Locate and identify every blood parasite.
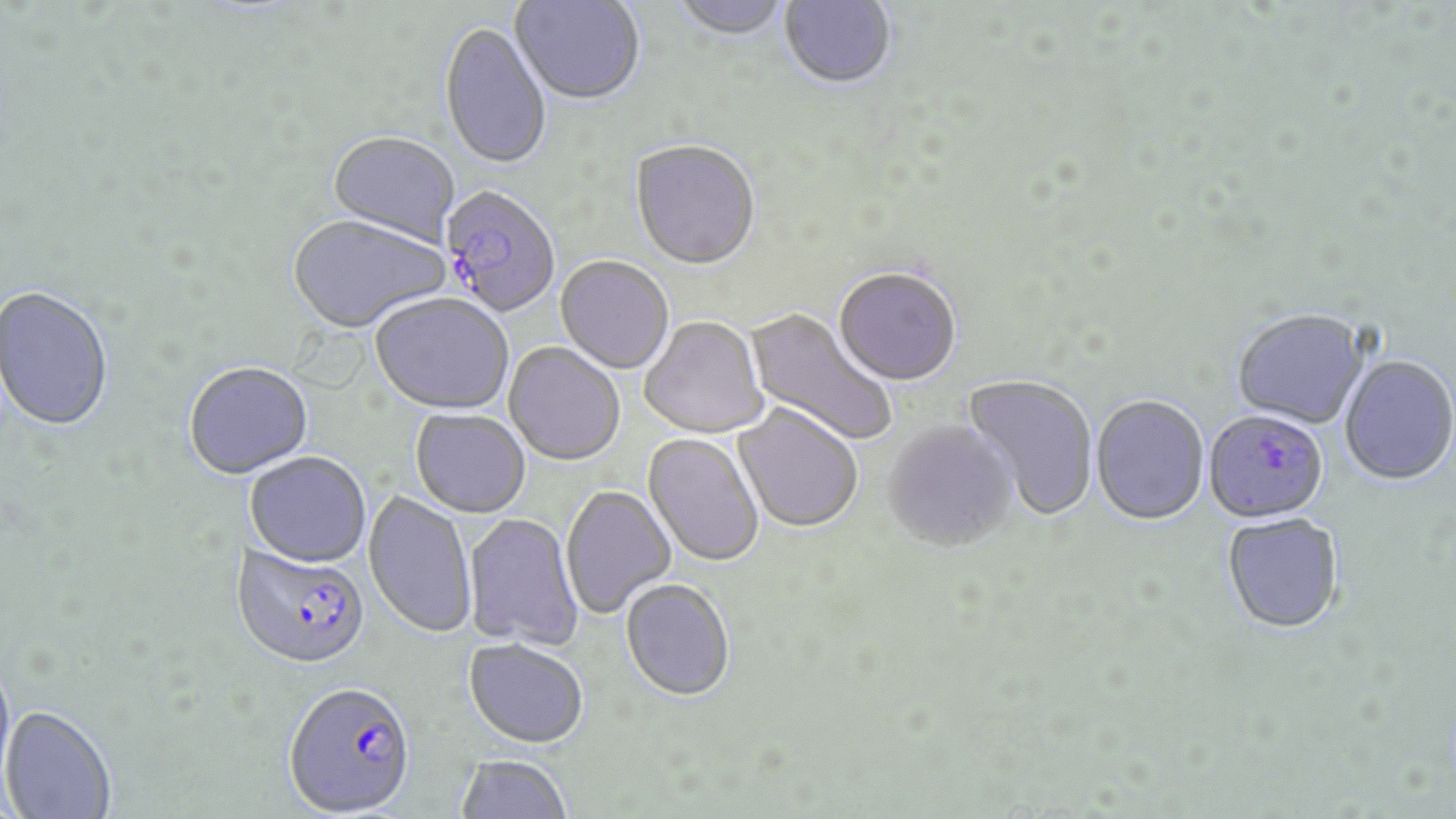
Approximate bounding boxes as (x1,y1)-(x2,y2) corner pairs in pixels.
Plasmodium falciparum-infected red blood cells: (439,186)-(561,318), (1203,410)-(1329,524), (231,544)-(370,669), (284,680)-(417,816).
No Plasmodium ovale, Plasmodium malariae, Plasmodium vivax, Babesia divergens, or Trypanosoma brucei observed.

Uninfected red blood cell locations: (510,0)-(645,107), (779,0)-(897,91), (670,1)-(792,43), (439,22)-(552,172), (326,133)-(459,249), (630,142)-(761,273), (287,216)-(449,336), (555,257)-(674,375), (834,268)-(962,387), (0,286)-(115,433), (370,295)-(514,416), (744,307)-(897,447), (1232,309)-(1370,429), (640,317)-(768,439), (503,343)-(625,467), (1339,354)-(1456,485), (183,363)-(314,481), (962,373)-(1099,522), (1091,395)-(1209,526), (732,404)-(864,534), (410,409)-(531,519), (883,421)-(1019,554), (643,433)-(764,568), (245,453)-(371,568), (560,485)-(676,619), (364,491)-(477,639), (462,513)-(583,649), (1221,513)-(1345,634), (620,580)-(735,703), (464,639)-(588,747), (0,656)-(16,800), (0,705)-(117,819), (454,753)-(574,819). Slide-level diagnosis: Plasmodium falciparum. 1000x magnification. Light microscopy. May-Grünwald-Giemsa-stained preparation. One field of a larger specimen. Image is 1456×819 pixels. Thin blood smear.